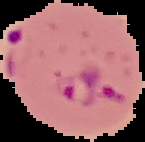
Summary:
  - Image size: 145×142 pixels
  - Preparation: thin blood film
  - Image type: segmented cell region on a black background
  - Malaria status: parasitized